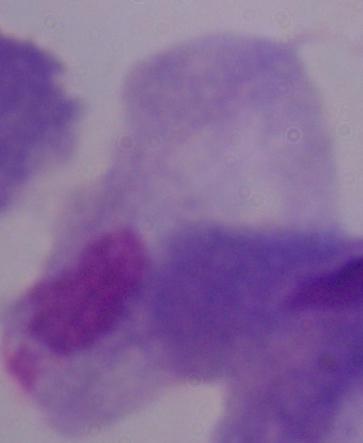

Summary:
  - Modality: micrograph
  - Magnification: 1000x
  - Identification: trichomonad